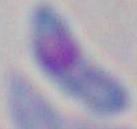 Photomicrograph. Toxoplasma gondii is shown. Captured at 1000x magnification.